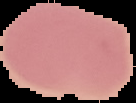
Image is 136×103 pixels. Segmented cell region on a black background. From a thin blood smear. Result: no Plasmodium parasites seen.